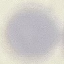
Malaria status: uninfected. Automatically extracted cell patch, resized to 64 × 64 pixels. Thin smear of blood. Photographed with a smartphone camera at the microscope eyepiece. Giemsa stain.